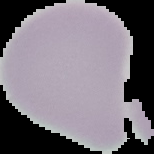
result: negative for Plasmodium parasites
image_size: 154×154 pixels
preparation: thin blood film
image_type: segmented cell region with the area outside set to black